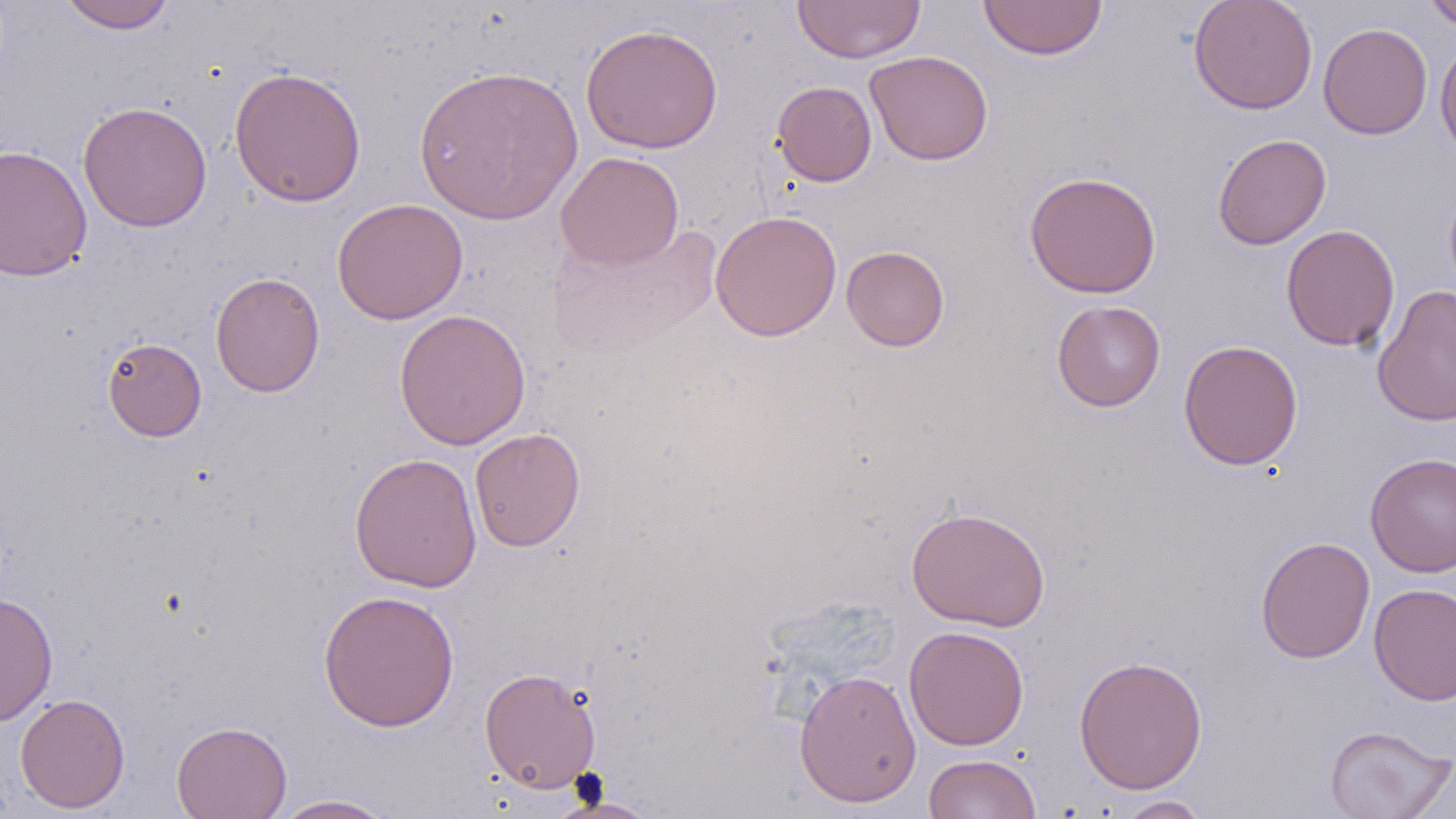

slide-level diagnosis = negative for blood parasites
image size = 1456×819 pixels
uninfected red blood cell locations = approximate bounding boxes as (x1,y1)-(x2,y2) corner pairs in pixels: (56,0)-(178,32), (792,0)-(926,64), (1188,0)-(1318,114), (1421,0)-(1456,31), (977,1)-(1108,60), (1318,22)-(1433,140), (580,24)-(723,154), (1435,40)-(1456,161), (864,50)-(993,166), (413,64)-(583,225), (229,66)-(367,208), (772,81)-(877,186), (78,101)-(212,232), (1213,133)-(1331,250), (0,143)-(93,282), (555,151)-(684,270), (1024,171)-(1162,299), (332,198)-(468,324), (710,210)-(842,341), (547,222)-(722,360), (1280,224)-(1400,352), (841,245)-(950,351), (210,272)-(325,397), (1372,285)-(1456,429), (1052,300)-(1166,411), (394,308)-(531,450), (102,337)-(207,442), (1178,339)-(1303,470), (469,428)-(585,552), (349,452)-(482,593), (1365,452)-(1456,577), (906,506)-(1051,632), (1255,536)-(1376,663), (1369,583)-(1456,706), (318,589)-(459,731), (1,592)-(58,726), (904,625)-(1030,750), (1073,654)-(1208,794), (479,667)-(601,793), (794,669)-(921,808), (14,693)-(130,814), (172,720)-(292,819), (1323,725)-(1455,819), (923,753)-(1042,819), (269,794)-(401,818), (1112,795)-(1212,818)
stain = May-Grünwald-Giemsa
preparation = thin blood film
field of view = one of a larger specimen
magnification = 1000x
modality = optical microscopy